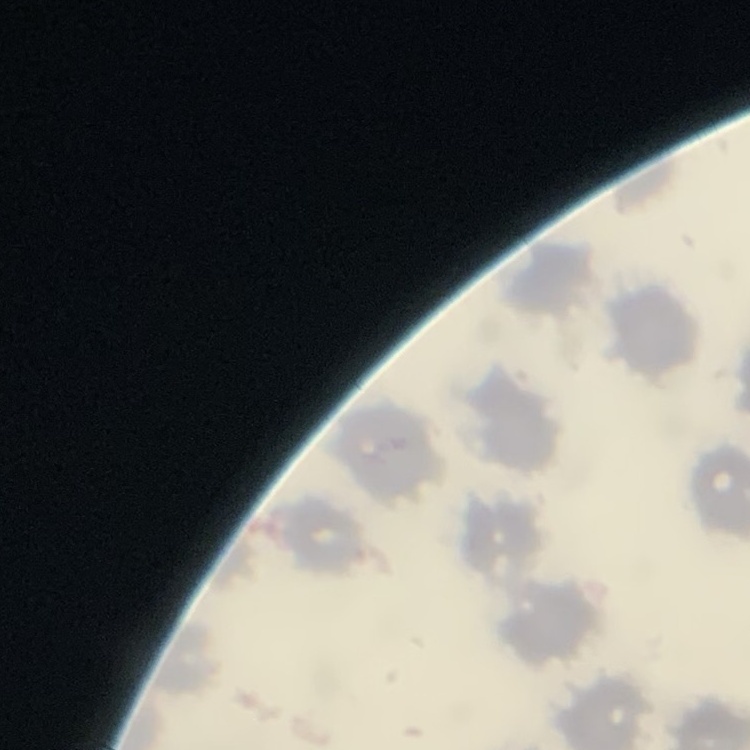
Summary:
  - Erythrocyte morphology: no rouleaux formation
  - Image type: square crop of a larger photomicrograph
  - Preparation: thin blood smear
  - Stain: Field's or Giemsa